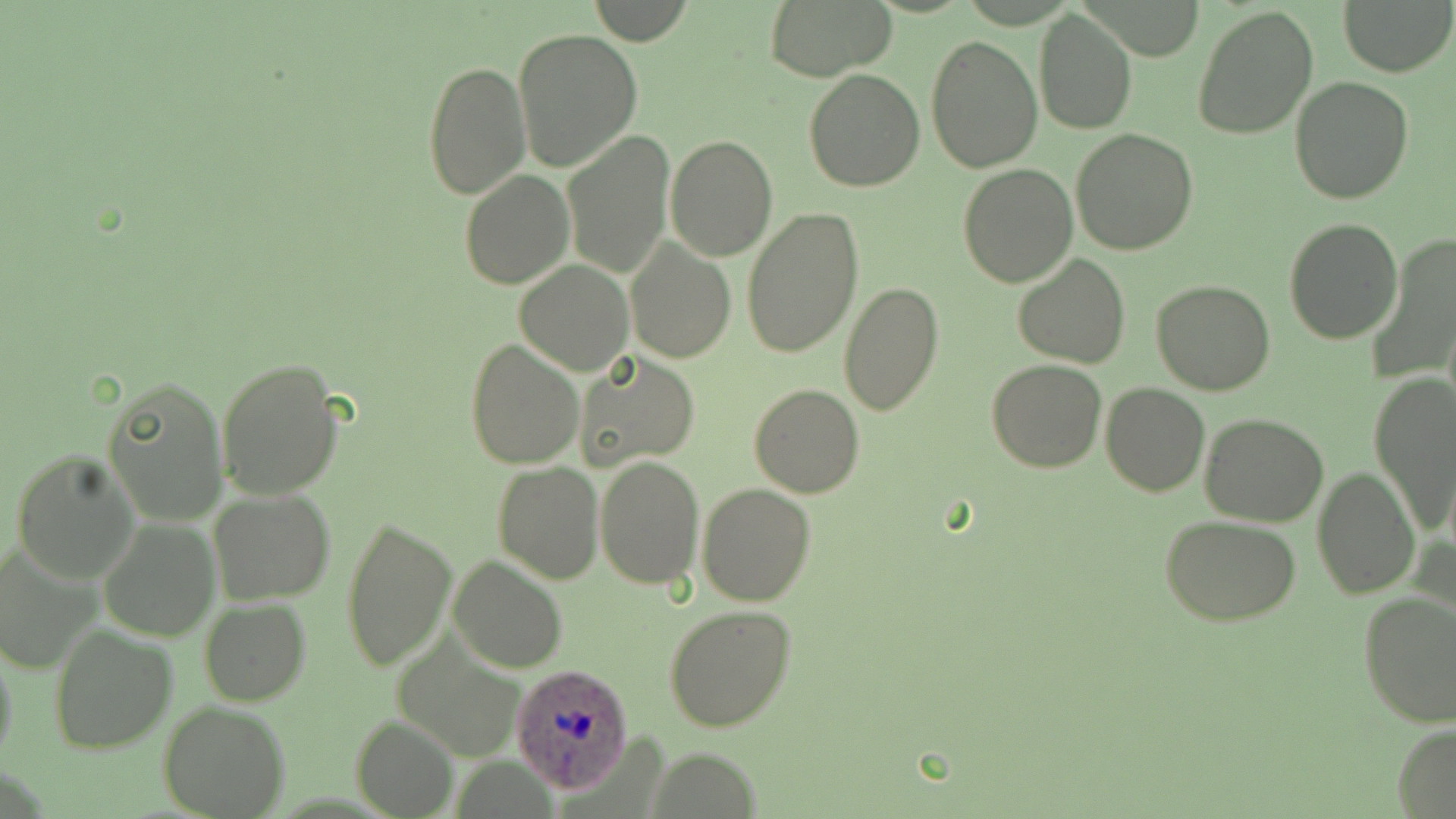

Summary:
  - Coordinate format: approximate bounding boxes as [x1, y1, x2, y2] in pixels
  - Uninfected red blood cell locations: [760, 0, 897, 80], [1340, 0, 1452, 76], [582, 2, 696, 43], [1191, 4, 1320, 140], [1033, 9, 1137, 135], [513, 27, 643, 173], [924, 34, 1043, 173], [421, 60, 531, 200], [804, 69, 926, 192], [1290, 78, 1413, 205], [1070, 128, 1199, 256], [561, 129, 675, 279], [665, 135, 778, 261], [957, 163, 1078, 287], [459, 170, 573, 289], [740, 205, 865, 360], [1283, 216, 1402, 343], [625, 236, 736, 365], [1367, 236, 1455, 388], [1012, 253, 1129, 369], [515, 260, 633, 377], [1150, 279, 1277, 396], [838, 280, 944, 416], [464, 337, 583, 469], [576, 351, 700, 471], [216, 358, 346, 502], [988, 360, 1108, 473], [1369, 371, 1456, 534], [102, 375, 229, 524], [1100, 381, 1210, 497], [749, 384, 866, 498], [1199, 413, 1330, 527], [11, 451, 140, 584], [594, 456, 704, 591], [493, 461, 604, 584], [1312, 467, 1420, 599], [696, 483, 816, 606], [209, 487, 334, 604], [339, 513, 458, 673], [1159, 514, 1303, 625], [98, 516, 219, 642], [0, 544, 103, 672], [448, 555, 566, 672], [1356, 591, 1456, 729], [199, 598, 311, 706], [663, 604, 797, 733], [50, 624, 177, 753], [0, 634, 19, 772], [158, 701, 291, 819], [353, 714, 458, 818], [1393, 725, 1456, 816]
  - Plasmodium ovale-infected red blood cell locations: [511, 663, 631, 795]
  - Slide-level diagnosis: Plasmodium ovale
  - Image size: 1456×819 pixels
  - Field of view: one of a larger specimen
  - Modality: optical microscopy
  - Stain: May-Grünwald-Giemsa
  - Magnification: 1000x
  - Preparation: thin blood film